Assess this cell for malaria.
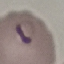
Parasitized.

{
  "capture": "smartphone through the microscope eyepiece",
  "stain": "Giemsa",
  "preparation": "thin smear",
  "image_type": "automatically extracted cell patch, resized to 64 × 64 pixels"
}